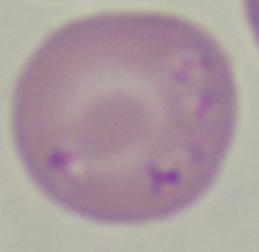

Summary:
  - Identification: Babesia
  - Modality: photomicrograph
  - Magnification: 1000x